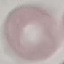

Summary:
  - Malaria status: uninfected
  - Preparation: thin blood smear
  - Stain: Giemsa
  - Capture: smartphone through the microscope eyepiece
  - Image type: automatically extracted cell patch, resized to 64 × 64 pixels